Report the malaria status of this cell.
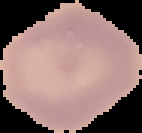

Uninfected.

image type = segmented cell region on a black background
preparation = thin blood smear
image size = 142×133 pixels